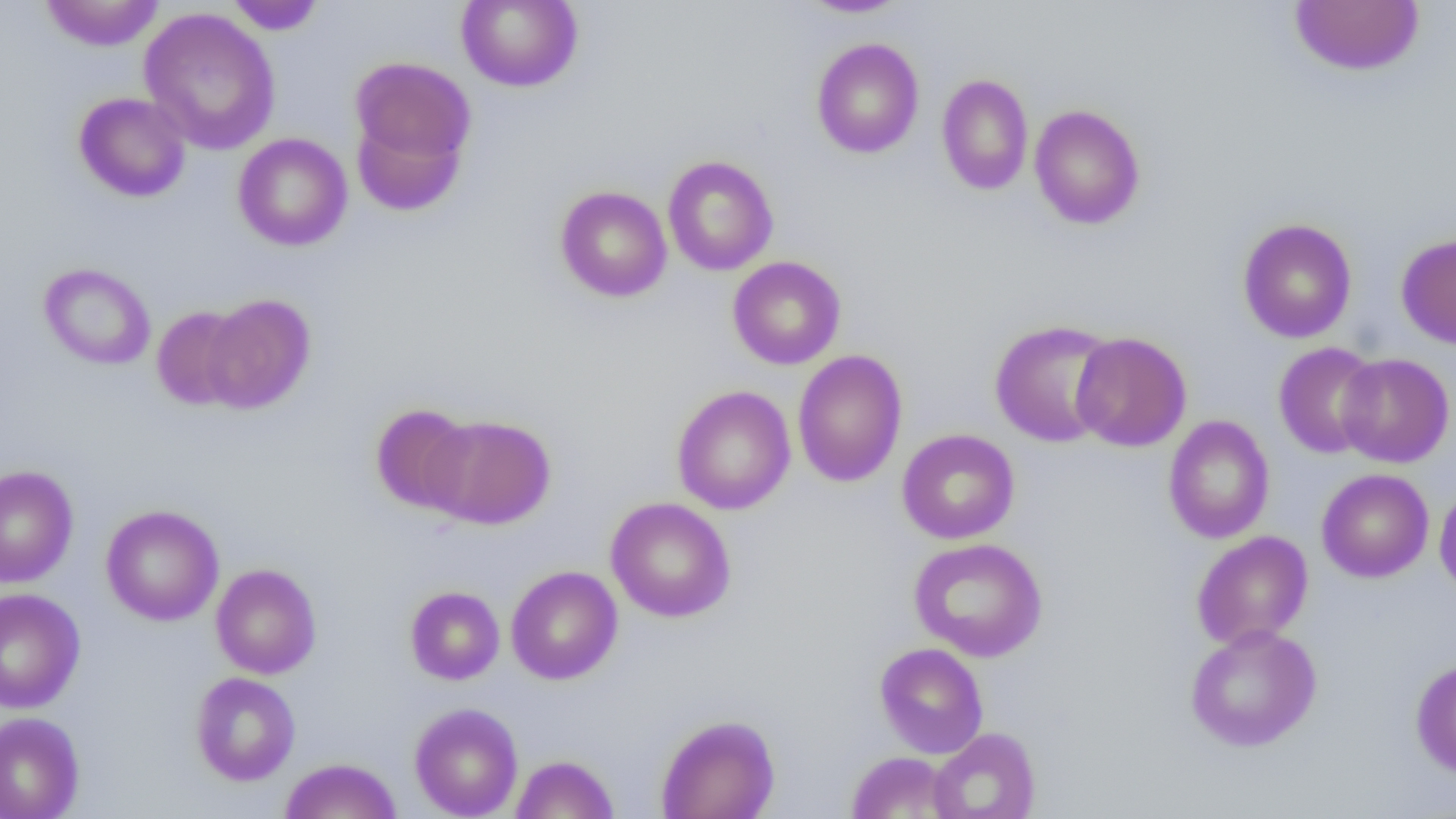

{
  "slide_level_diagnosis": "no evidence of blood parasites",
  "modality": "optical microscopy",
  "image_size": "1456×819 pixels",
  "uninfected_red_blood_cell_locations": "approximate bounding boxes as (x1,y1)-(x2,y2) corner pairs in pixels: (39,1)-(165,51), (225,1)-(326,35), (457,1)-(583,91), (799,1)-(910,17), (1289,1)-(1425,76), (139,8)-(281,155), (811,38)-(924,158), (349,55)-(476,181), (936,73)-(1033,195), (73,92)-(191,202), (1029,104)-(1145,230), (232,133)-(352,251), (663,155)-(778,276), (556,186)-(672,302), (1238,218)-(1357,343), (1396,233)-(1456,350), (727,256)-(846,370), (38,263)-(156,370), (202,294)-(316,414), (151,306)-(250,410), (989,319)-(1119,447), (1070,331)-(1192,452), (1273,342)-(1384,459), (792,349)-(908,487), (1336,352)-(1454,468), (672,385)-(796,515), (370,403)-(477,515), (425,415)-(556,529), (1162,415)-(1275,543), (897,429)-(1020,544), (0,464)-(78,587), (1317,469)-(1434,583), (1434,483)-(1456,598), (606,497)-(736,622), (101,504)-(224,626), (1191,530)-(1313,650), (908,538)-(1048,662), (211,563)-(321,679), (505,566)-(622,685), (405,585)-(504,685), (0,588)-(85,713), (1185,624)-(1322,752), (874,642)-(988,758), (1410,658)-(1456,778), (190,672)-(301,786), (410,703)-(523,819), (0,712)-(85,819), (656,713)-(780,819), (928,727)-(1041,818), (847,751)-(957,818), (511,754)-(619,818), (279,758)-(401,819)",
  "field_of_view": "single",
  "preparation": "thin blood smear",
  "magnification": "1000x"
}